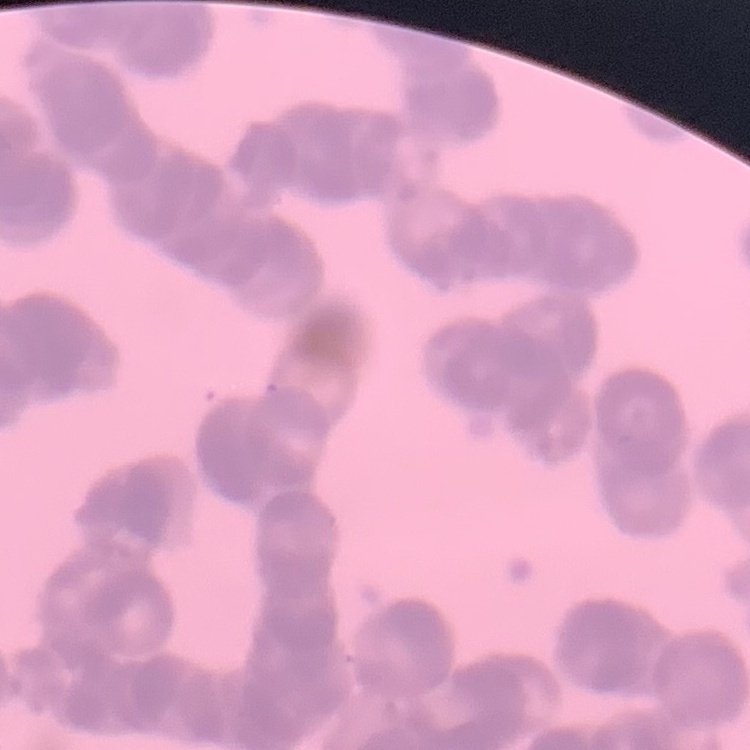

{
  "erythrocyte_morphology": "rouleaux formation",
  "image_type": "one tile cut from a larger photomicrograph",
  "stain": "Field's or Giemsa",
  "preparation": "thin blood smear"
}